Comment on the morphology of the red blood cells.
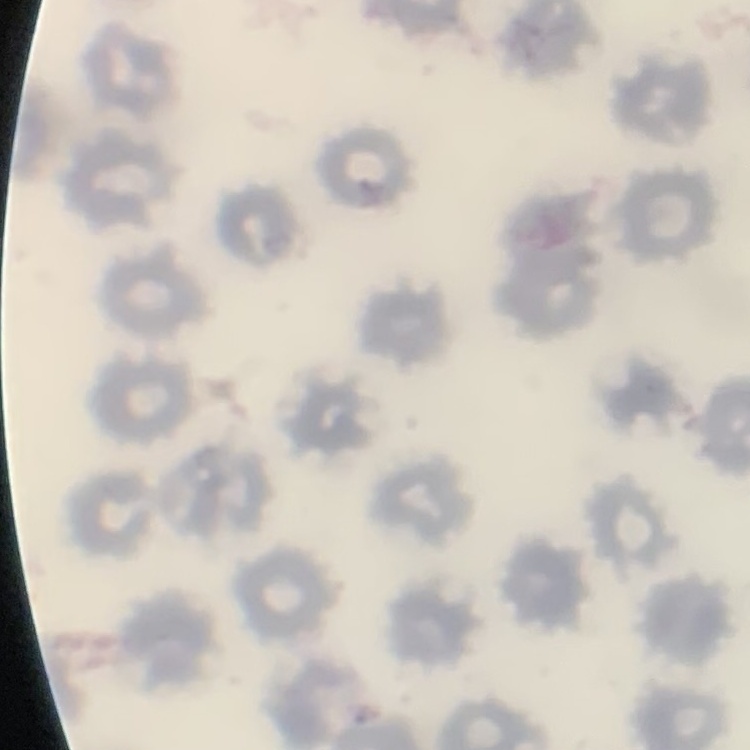
No rouleaux formation.

Field's or Giemsa stain. One tile cut from a larger photomicrograph. Thin blood smear.